State which parasite is depicted.
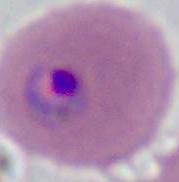
Plasmodium.

Summary:
  - Magnification: 400x or 1000x
  - Modality: photomicrograph